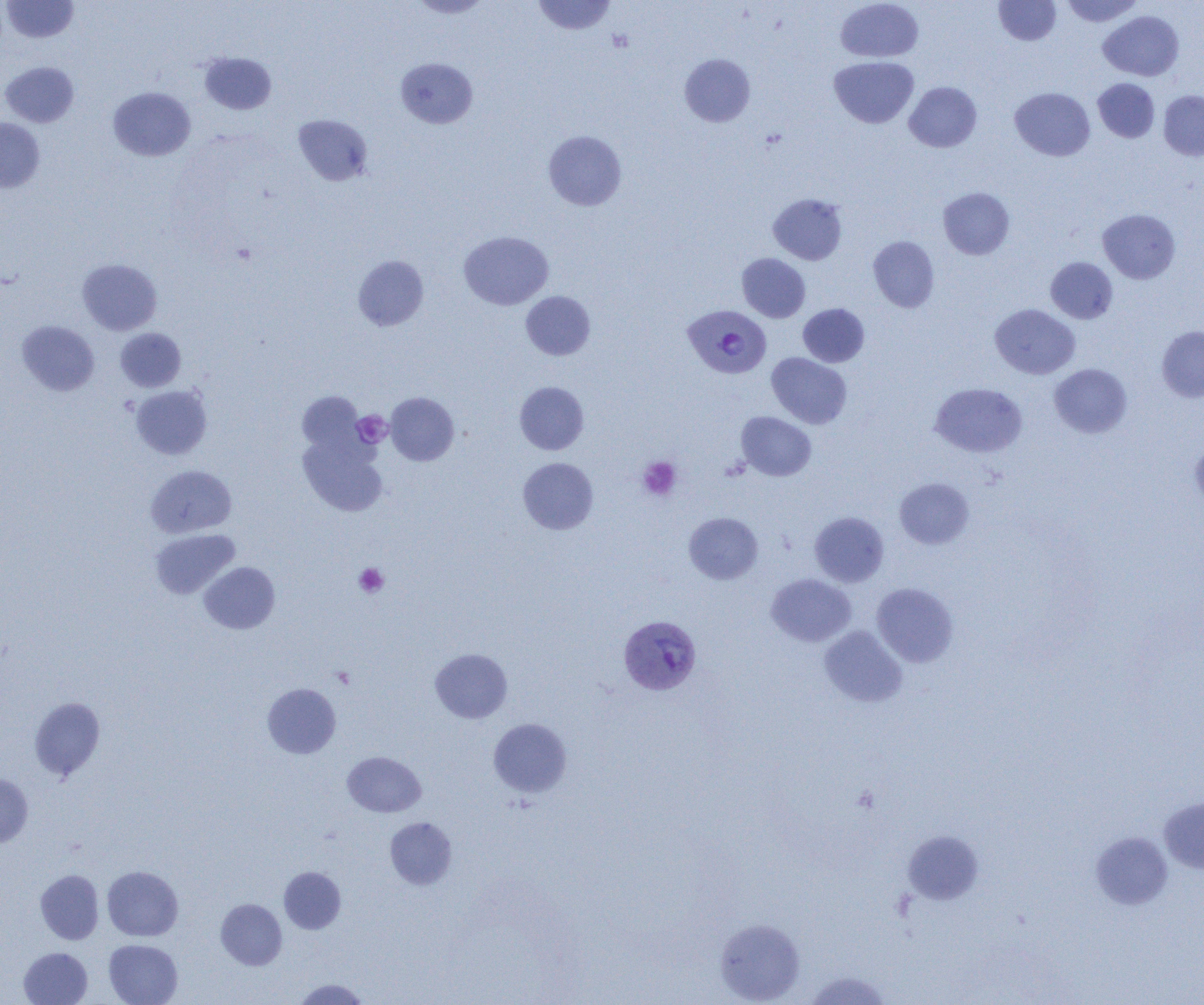

slide-level diagnosis = Plasmodium vivax
image size = 1204×1005 pixels
modality = light microscopy
uninfected red blood cell locations = approximate bounding boxes as (x1, y1, x2, y2) in pixels: (2, 0, 79, 43), (407, 0, 493, 18), (532, 0, 616, 35), (993, 0, 1061, 45), (1060, 0, 1144, 27), (835, 1, 923, 62), (1099, 10, 1184, 80), (199, 52, 277, 114), (680, 53, 755, 127), (829, 56, 919, 128), (395, 58, 477, 128), (0, 61, 79, 127), (1093, 78, 1160, 143), (904, 81, 982, 152), (108, 87, 196, 161), (1010, 87, 1095, 161), (1159, 90, 1204, 160), (293, 114, 373, 186), (0, 118, 45, 192), (543, 130, 627, 211), (938, 187, 1014, 259), (768, 193, 847, 264), (1097, 209, 1180, 284), (459, 231, 553, 309), (868, 236, 939, 312), (737, 253, 810, 322), (353, 255, 429, 331), (1046, 257, 1117, 324), (77, 259, 162, 335), (521, 291, 595, 360), (798, 304, 869, 367), (990, 304, 1080, 379), (17, 321, 99, 396), (1157, 326, 1204, 402), (115, 328, 186, 391), (766, 352, 852, 428), (1049, 364, 1132, 438), (515, 381, 589, 454), (930, 382, 1027, 457), (130, 385, 212, 460), (297, 391, 366, 456), (385, 392, 459, 466), (736, 411, 816, 481), (298, 433, 388, 517), (1190, 438, 1204, 511), (518, 457, 598, 534), (146, 465, 237, 537), (894, 478, 974, 549), (684, 512, 763, 584), (809, 512, 889, 587), (150, 528, 240, 598), (199, 562, 280, 634), (766, 573, 856, 647), (871, 583, 959, 667), (819, 626, 907, 707), (430, 648, 513, 723), (262, 683, 341, 758), (29, 697, 105, 781), (488, 718, 572, 797), (342, 751, 426, 817), (0, 773, 33, 847), (1158, 797, 1204, 874), (385, 817, 457, 890), (903, 830, 983, 904), (1091, 832, 1173, 910), (102, 866, 183, 941), (279, 866, 346, 934), (35, 870, 104, 944), (216, 898, 287, 970), (715, 918, 805, 1004), (104, 939, 183, 1005), (19, 947, 93, 1005), (803, 971, 893, 1004), (293, 978, 370, 1004)
preparation = thin blood film
platelet locations = approximate bounding boxes as (x1, y1, x2, y2) in pixels: (353, 411, 392, 448), (638, 456, 682, 500), (354, 563, 388, 597)
field of view = single
magnification = 1000x
Plasmodium vivax-infected red blood cell locations = approximate bounding boxes as (x1, y1, x2, y2) in pixels: (683, 305, 772, 379), (619, 615, 702, 694)